Classify this cell by malaria status.
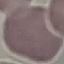

Uninfected.

stain: Giemsa
capture: smartphone through the microscope eyepiece
image_type: cell patch, automatically extracted from a larger field of view and resized to 64 × 64 pixels
preparation: thin blood smear